Report the malaria status of this cell.
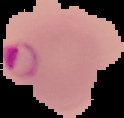
It is parasitized.

preparation = thin blood smear
image size = 124×118 pixels
image type = segmented cell region with the area outside set to black